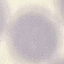

Result: no malaria parasites detected. Giemsa stain. Thin smear of blood. Photographed with a smartphone camera at the microscope eyepiece. Automatically extracted cell patch, resized to 64 × 64 pixels.